Report the malaria status of this cell.
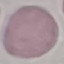
Uninfected.

Summary:
  - Stain: Giemsa
  - Image type: automatically extracted cell patch, resized to 64 × 64 pixels
  - Preparation: thin blood smear
  - Capture: smartphone camera at the microscope eyepiece